Comment on the morphology of the erythrocytes.
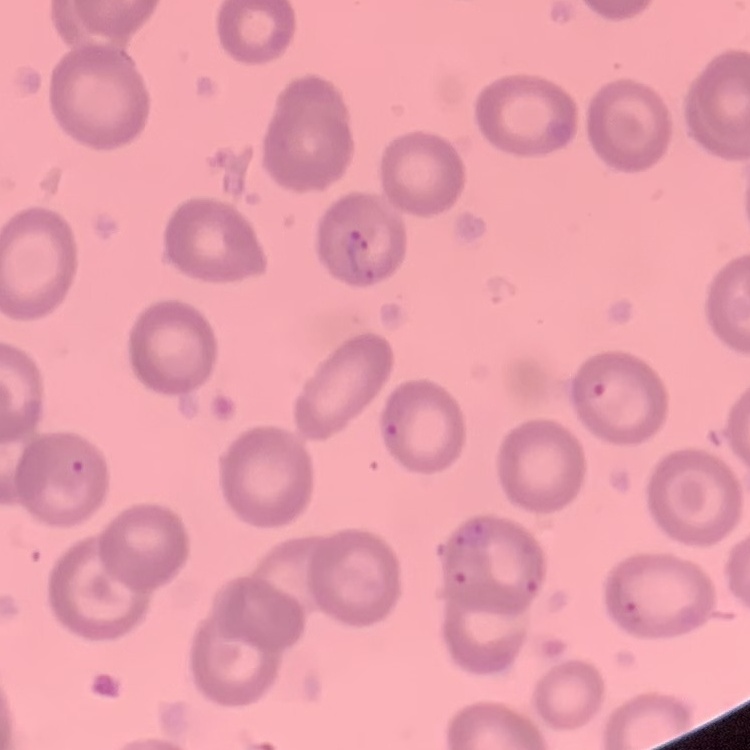
No rouleaux formation.

Summary:
  - Preparation: thin peripheral smear
  - Stain: Field's or Giemsa
  - Image type: square crop of a larger photomicrograph